Assess the morphology of the red blood cells.
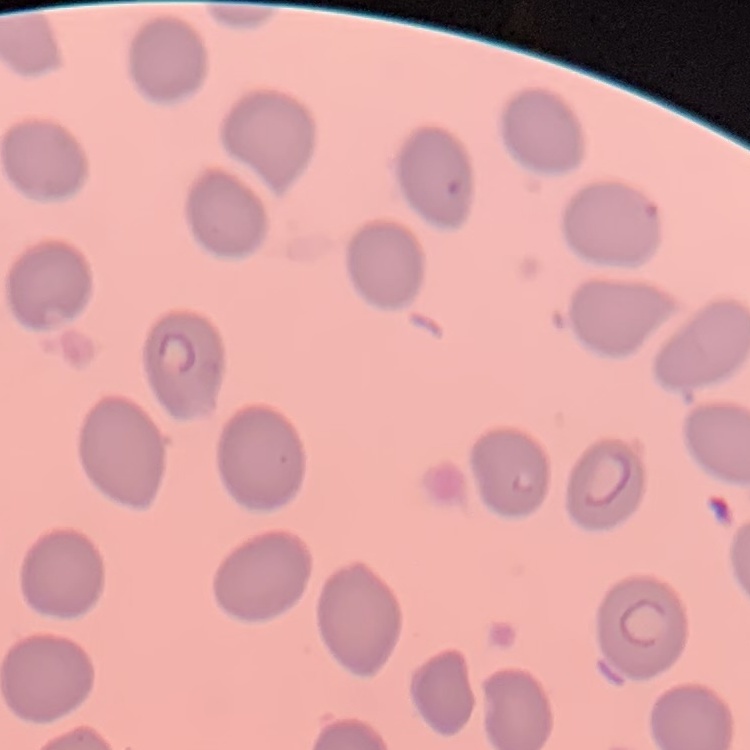

They show no rouleaux formation.

Summary:
  - Preparation: thin blood film
  - Image type: square crop of a larger photomicrograph
  - Stain: Field's or Giemsa